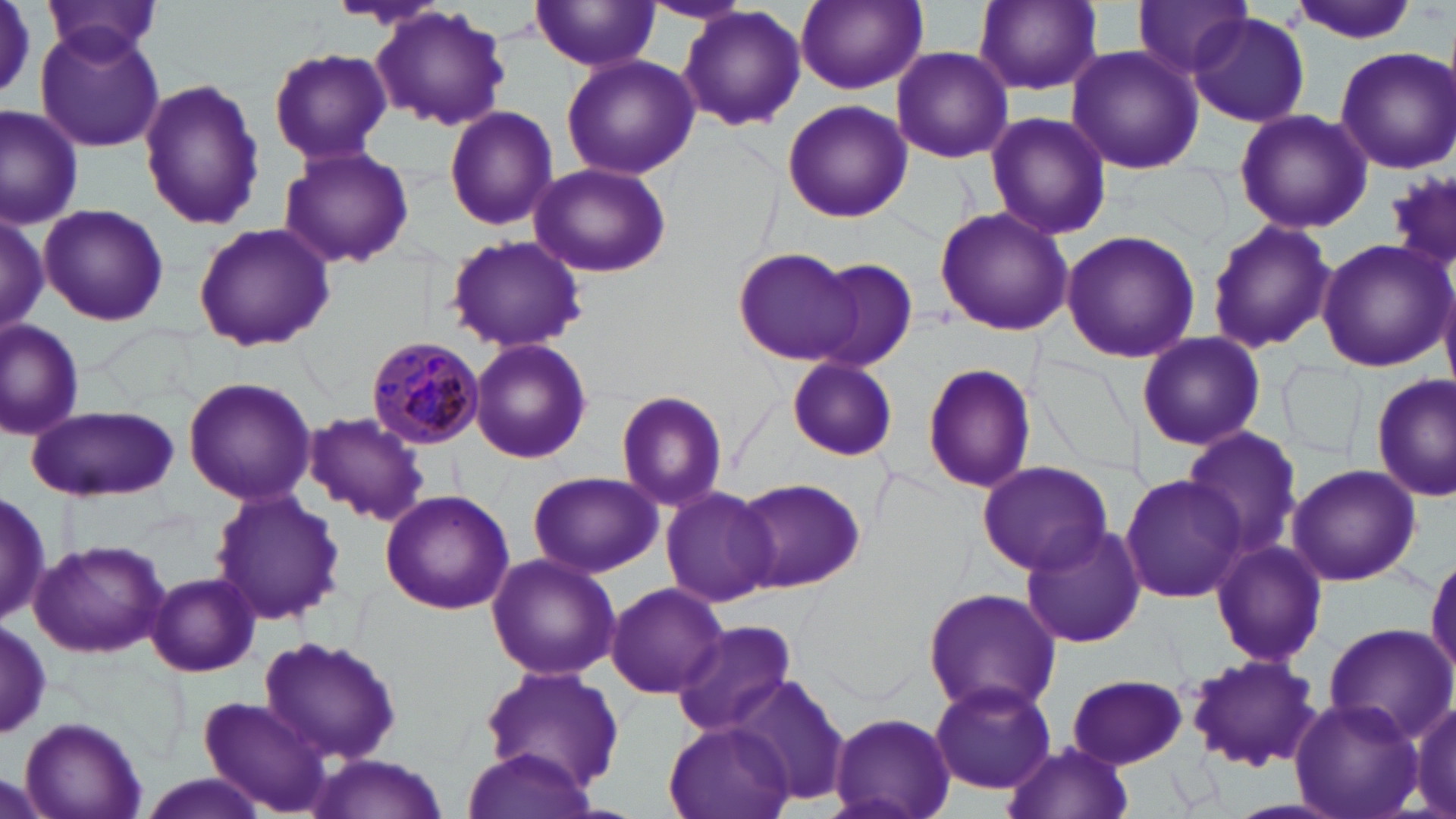

Approximate bounding boxes as (x1,y1)-(x2,y2) corner pairs in pixels. Uninfected red blood cell locations: (0,0)-(55,109), (42,0)-(165,69), (795,0)-(927,93), (975,0)-(1101,94), (641,1)-(752,28), (1287,1)-(1424,42), (530,2)-(662,72), (1131,2)-(1254,82), (371,7)-(511,132), (677,7)-(807,134), (1186,13)-(1310,127), (34,25)-(167,151), (1065,45)-(1205,175), (1332,45)-(1456,175), (269,47)-(391,165), (891,47)-(1013,165), (561,54)-(701,180), (139,79)-(264,232), (780,99)-(913,224), (1,104)-(84,227), (444,105)-(557,230), (1233,108)-(1372,232), (983,111)-(1113,243), (278,146)-(415,269), (529,163)-(671,277), (39,203)-(167,325), (934,206)-(1073,338), (0,211)-(48,337), (1205,218)-(1334,356), (192,222)-(335,352), (1061,230)-(1202,363), (444,234)-(587,352), (1318,237)-(1452,371), (732,245)-(865,364), (806,257)-(921,370), (0,320)-(83,443), (1138,330)-(1266,451), (468,339)-(593,465), (785,355)-(898,462), (1281,359)-(1365,464), (921,361)-(1037,495), (1372,374)-(1455,503), (182,377)-(317,506), (615,389)-(730,511), (26,404)-(179,501), (304,412)-(431,527), (1181,428)-(1305,561), (975,461)-(1111,575), (1286,463)-(1422,587), (526,471)-(662,579), (1122,473)-(1248,603), (730,475)-(866,594), (0,484)-(51,624), (660,484)-(775,606), (210,487)-(343,626), (378,488)-(516,614), (1018,522)-(1146,649), (28,538)-(171,659), (1210,539)-(1327,667), (1427,548)-(1456,683), (486,554)-(621,682), (146,573)-(260,677), (606,581)-(728,698), (922,586)-(1061,718), (670,621)-(799,737), (1322,623)-(1454,744), (258,637)-(403,767), (1184,654)-(1323,773), (480,667)-(625,793), (1066,674)-(1189,769), (727,675)-(853,809), (927,682)-(1056,793), (199,696)-(330,814), (1400,696)-(1456,819), (1291,697)-(1422,819), (829,710)-(956,817), (16,715)-(146,819), (664,722)-(796,818), (1004,740)-(1132,819), (461,745)-(597,819), (305,751)-(452,818), (130,775)-(273,819). Plasmodium malariae-infected red blood cell locations: (365,335)-(485,447). Slide-level diagnosis: Plasmodium malariae. 1000x magnification. May-Grünwald-Giemsa-stained preparation. Optical microscopy. One field of a larger specimen. Thin blood smear. Image is 1456×819 pixels.